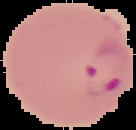

Cell region segmented out of the field of view; the surrounding area is masked to black. Malaria status: parasitized. From a thin blood film. Image is 136×130 pixels.